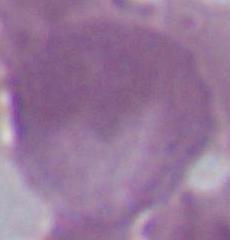

modality = photomicrograph
magnification = 1000x
identification = erythrocyte